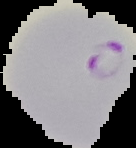

image_size: 136×148 pixels
result: malaria parasites detected
image_type: cell region segmented out of the field of view; surrounding area masked to black
preparation: thin blood film